Classify this cell by malaria status.
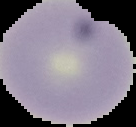

Uninfected.

Image is 136×127 pixels. Cell region segmented out of the field of view; the surrounding area is masked to black. From a thin blood film.